Report the malaria status of this cell.
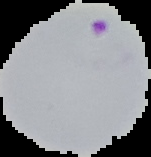
It is parasitized.

Image is 151×157 pixels. From a thin blood smear. Cell region segmented out of the field of view; the surrounding area is masked to black.